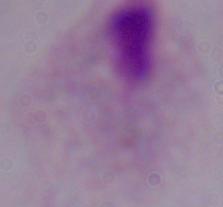 Photomicrograph. A trichomonad is seen. Captured at 1000x magnification.